Report the malaria status of this cell.
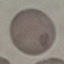

It is uninfected.

Summary:
  - Preparation: thin smear
  - Stain: Giemsa
  - Capture: smartphone camera at the microscope eyepiece
  - Image type: automatically extracted cell patch, resized to 64 × 64 pixels